Describe the morphology of the red blood cells.
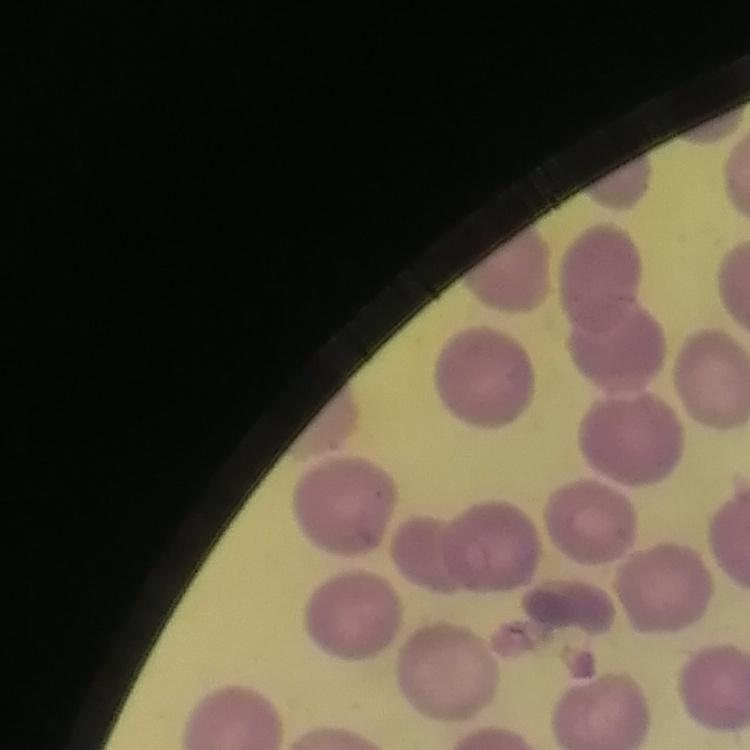
No rouleaux formation.

Summary:
  - Image type: square crop of a larger photomicrograph
  - Stain: Field's or Giemsa
  - Preparation: thin blood film